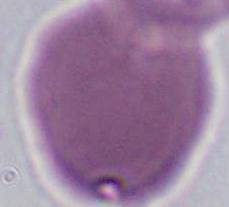

Summary:
  - Identification: red blood cell
  - Modality: micrograph
  - Magnification: 1000x